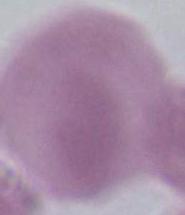
magnification = 1000x
modality = photomicrograph
identification = red blood cell